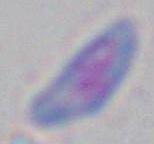
Summary:
  - Identification: Toxoplasma gondii
  - Magnification: 1000x
  - Modality: photomicrograph